Assess this cell for malaria.
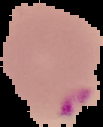

It is parasitized.

preparation: thin blood film
image_size: 103×127 pixels
image_type: cell region segmented out of the field of view; surrounding area masked to black